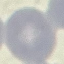

malaria status = uninfected
capture = smartphone through the microscope eyepiece
stain = Giemsa
image type = cell patch, automatically extracted from a larger field of view and resized to 64 × 64 pixels
preparation = thin blood smear